Classify this cell by malaria status.
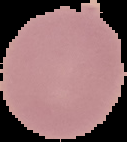

Uninfected.

image size = 127×142 pixels
image type = segmented cell region on a black background
preparation = thin blood film